Outline each Plasmodium vivax-infected red blood cell.
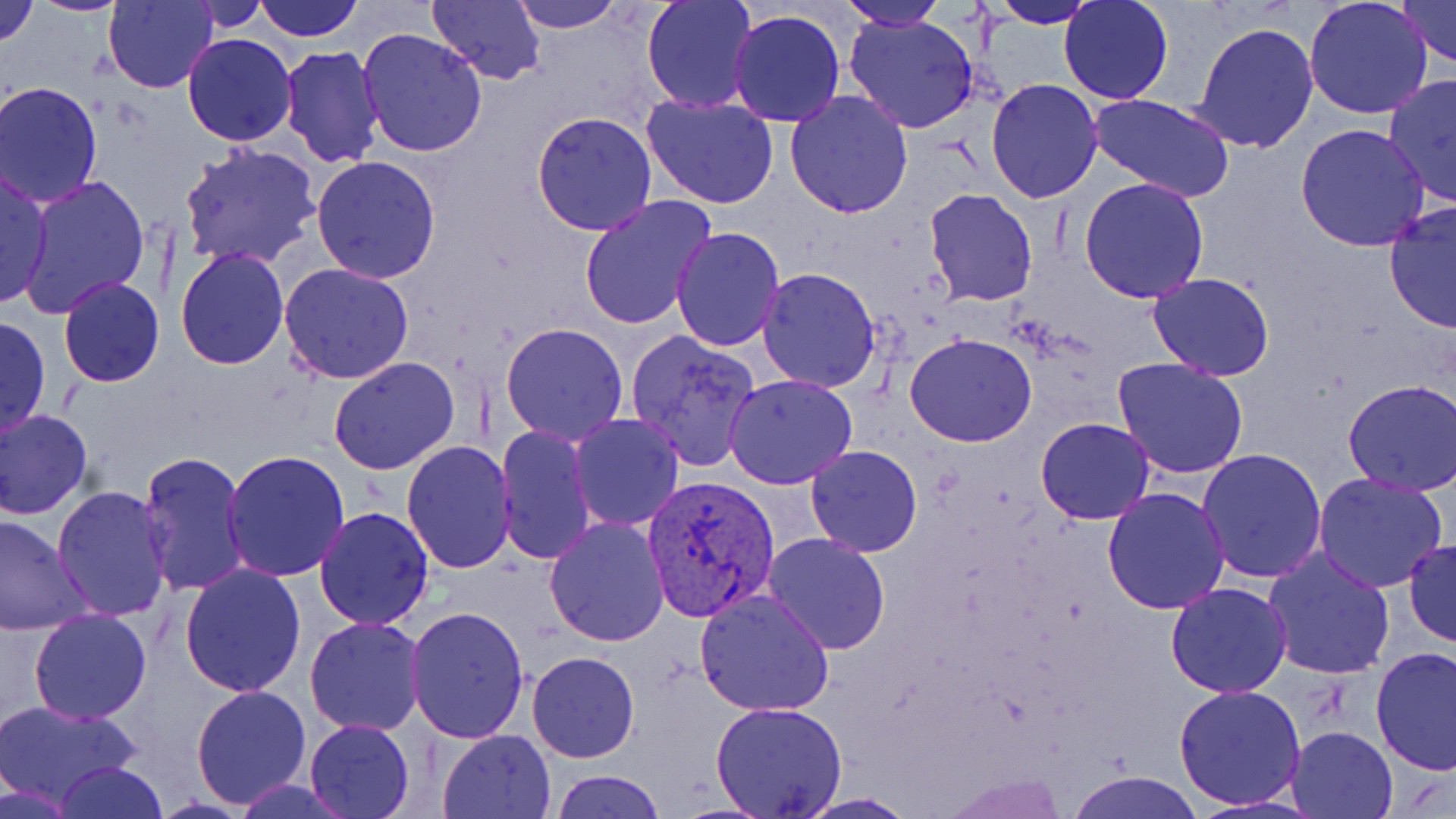

Approximate bounding boxes as [x1, y1, x2, y2] in pixels.
Plasmodium vivax-infected red blood cells: [641, 473, 780, 621].

Uninfected red blood cell locations: [0, 0, 39, 49], [28, 0, 134, 16], [104, 0, 218, 92], [184, 0, 270, 32], [254, 0, 362, 41], [427, 0, 545, 86], [509, 0, 622, 33], [642, 0, 758, 111], [985, 0, 1103, 28], [1303, 0, 1434, 120], [1397, 0, 1455, 70], [837, 1, 946, 31], [1058, 1, 1174, 103], [727, 9, 847, 127], [842, 12, 983, 135], [1191, 21, 1320, 154], [358, 27, 489, 158], [182, 33, 298, 146], [279, 46, 388, 169], [1382, 74, 1456, 210], [985, 80, 1105, 203], [1, 82, 104, 209], [784, 90, 914, 217], [641, 91, 780, 208], [1088, 94, 1236, 204], [531, 111, 658, 235], [1295, 123, 1430, 250], [180, 142, 322, 270], [310, 155, 442, 285], [0, 169, 53, 309], [15, 174, 153, 319], [1079, 177, 1210, 301], [924, 188, 1039, 307], [578, 195, 717, 328], [1383, 203, 1456, 336], [671, 226, 786, 352], [667, 243, 877, 370], [174, 247, 289, 369], [278, 263, 415, 384], [756, 266, 884, 393], [1149, 272, 1275, 380], [57, 277, 166, 388], [0, 313, 51, 437], [500, 321, 630, 445], [624, 329, 763, 473], [904, 332, 1037, 448], [328, 357, 460, 476], [1113, 358, 1249, 478], [723, 374, 858, 491], [1339, 380, 1456, 496], [1, 407, 93, 521], [569, 414, 685, 531], [1035, 417, 1155, 525], [494, 424, 597, 565], [402, 440, 518, 574], [805, 444, 923, 557], [1196, 448, 1328, 583], [221, 449, 350, 581], [139, 451, 251, 597], [1312, 473, 1451, 593], [51, 485, 175, 621], [1101, 487, 1231, 614], [313, 506, 435, 629], [0, 513, 90, 636], [544, 517, 672, 647], [761, 533, 891, 656], [1404, 538, 1455, 648], [1263, 547, 1396, 680], [179, 563, 307, 698], [1164, 581, 1294, 698], [694, 590, 837, 717], [405, 604, 530, 744], [28, 608, 152, 724], [304, 616, 426, 737], [1370, 646, 1455, 774], [526, 650, 640, 764], [190, 683, 311, 810], [1174, 683, 1307, 810], [0, 699, 144, 810], [710, 701, 848, 818], [303, 719, 414, 819], [1285, 725, 1400, 818], [437, 729, 555, 817], [55, 762, 167, 819], [550, 770, 665, 819], [1071, 771, 1200, 819], [793, 794, 920, 818]. Slide-level diagnosis: Plasmodium vivax. One field of a larger specimen. May-Grünwald-Giemsa-stained preparation. Image is 1456×819 pixels. Thin blood smear. Optical microscopy. Captured at 1000x magnification.